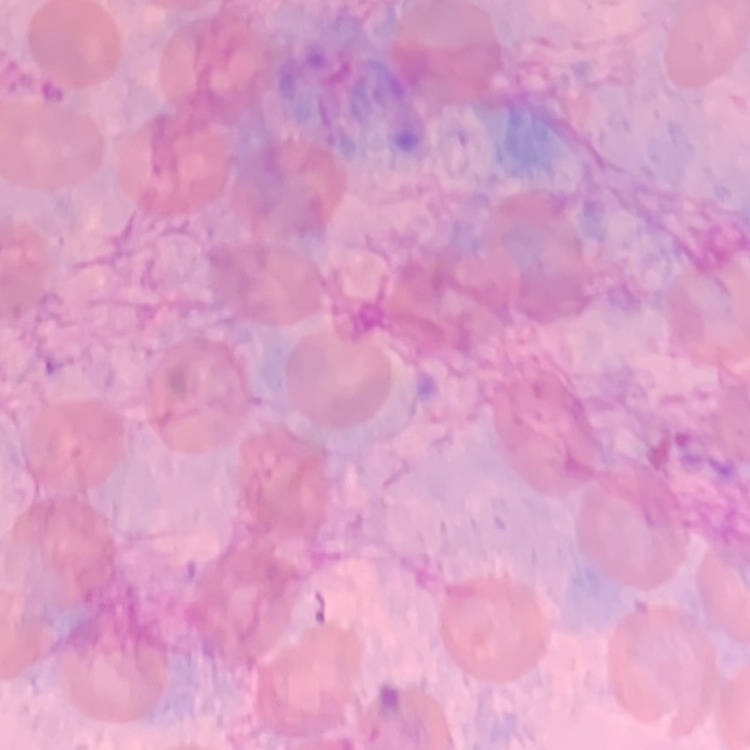
erythrocyte morphology = no rouleaux formation
stain = Field's or Giemsa
image type = square crop of a larger photomicrograph
preparation = thin blood smear